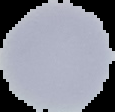

result = no Plasmodium parasites seen
image type = cell region segmented out of the field of view; surrounding area masked to black
preparation = thin blood smear
image size = 115×112 pixels